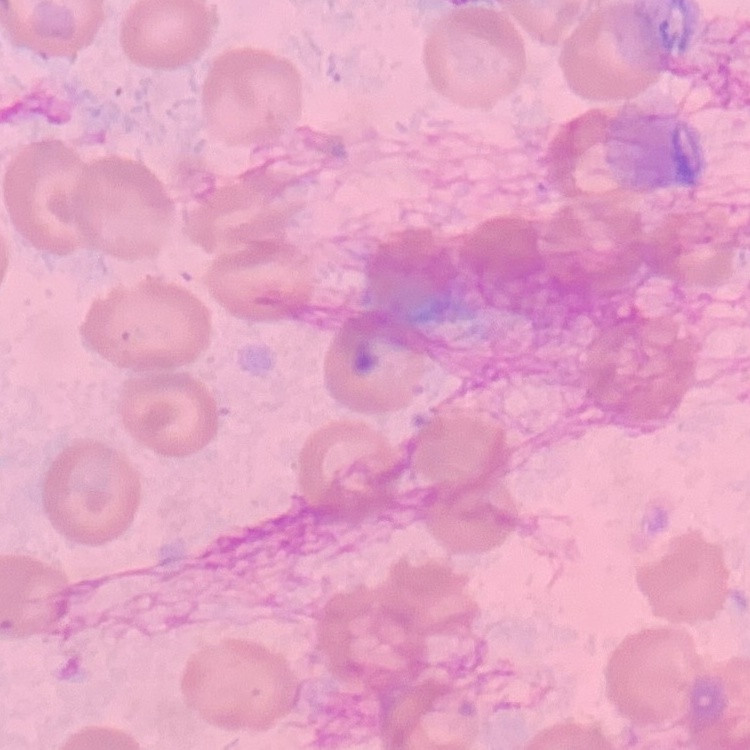

{
  "erythrocyte_morphology": "no rouleaux formation",
  "image_type": "square crop of a larger photomicrograph",
  "stain": "Field's or Giemsa",
  "preparation": "thin peripheral smear"
}